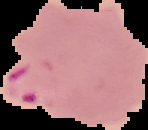
From a thin blood film. Image is 148×130 pixels. Malaria status: parasitized. Cell region segmented out of the field of view; the surrounding area is masked to black.